Identify the blood parasite species.
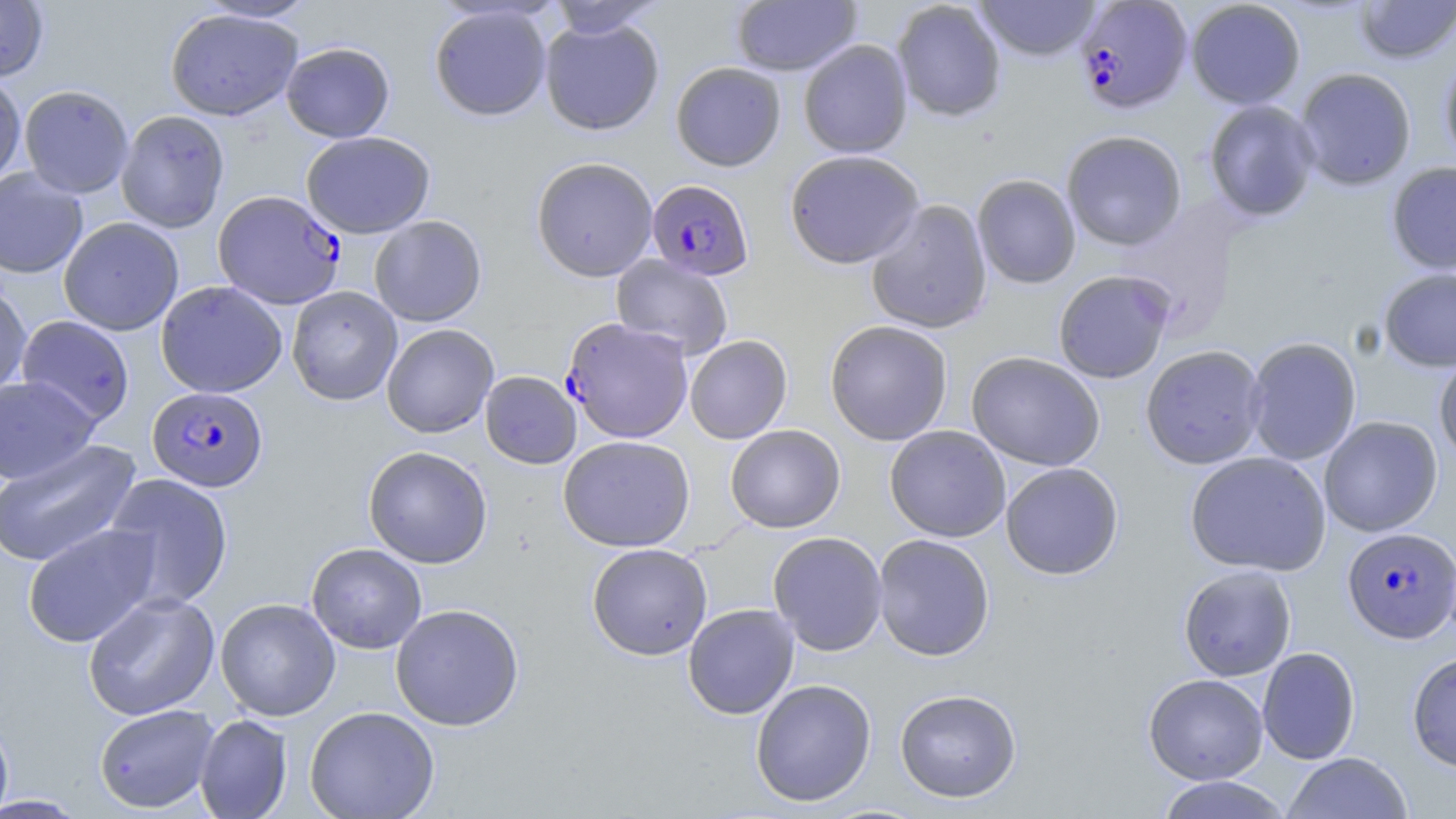

Plasmodium falciparum.

Summary:
  - Coordinate format: approximate bounding boxes as [x1, y1, x2, y2] in pixels
  - Plasmodium falciparum-infected red blood cell locations: [1074, 0, 1193, 114], [645, 179, 753, 281], [212, 190, 345, 310], [562, 318, 693, 444], [147, 386, 268, 492], [1342, 528, 1456, 644]
  - Uninfected red blood cell locations: [195, 0, 317, 23], [731, 0, 862, 76], [892, 0, 1007, 122], [973, 0, 1101, 62], [1186, 0, 1305, 109], [1354, 0, 1455, 64], [0, 1, 49, 81], [546, 1, 666, 38], [429, 4, 552, 121], [165, 9, 303, 121], [539, 17, 664, 136], [798, 39, 912, 158], [281, 42, 395, 142], [1439, 54, 1456, 169], [671, 61, 786, 172], [1294, 68, 1416, 190], [0, 72, 26, 186], [19, 85, 134, 198], [1203, 99, 1320, 222], [116, 110, 230, 232], [1061, 130, 1187, 251], [301, 131, 435, 238], [784, 150, 925, 269], [531, 157, 658, 282], [1386, 162, 1456, 274], [0, 167, 88, 278], [972, 174, 1081, 289], [866, 200, 992, 335], [369, 215, 487, 327], [59, 217, 184, 335], [611, 254, 733, 360], [1378, 268, 1456, 372], [1053, 270, 1176, 384], [156, 281, 288, 398], [0, 282, 32, 400], [286, 286, 402, 406], [17, 315, 134, 427], [824, 320, 953, 446], [381, 323, 499, 438], [684, 335, 793, 444], [1245, 337, 1361, 465], [1140, 344, 1266, 469], [966, 352, 1105, 471], [1434, 352, 1456, 465], [480, 371, 581, 469], [0, 375, 100, 484], [1319, 416, 1443, 537], [725, 424, 846, 533], [884, 425, 1011, 542], [558, 435, 695, 552], [0, 439, 142, 568], [363, 445, 493, 569], [1185, 451, 1331, 577], [1000, 462, 1124, 580], [103, 473, 234, 611], [23, 523, 161, 648], [768, 531, 888, 656], [873, 534, 995, 661], [306, 542, 427, 654], [586, 543, 712, 660], [1178, 565, 1297, 681], [82, 591, 220, 721], [215, 597, 341, 721], [683, 603, 799, 719], [390, 604, 524, 731], [1257, 647, 1360, 765], [1407, 651, 1456, 772], [1143, 673, 1268, 784], [750, 679, 876, 807], [894, 688, 1022, 803], [94, 704, 219, 813], [304, 705, 440, 819], [194, 714, 293, 819], [0, 715, 14, 818], [1283, 752, 1412, 818], [1155, 776, 1291, 819], [0, 795, 89, 817]
  - Stain: May-Grünwald-Giemsa
  - Magnification: 1000x
  - Image size: 1456×819 pixels
  - Modality: optical microscopy
  - Field of view: single
  - Preparation: thin blood smear